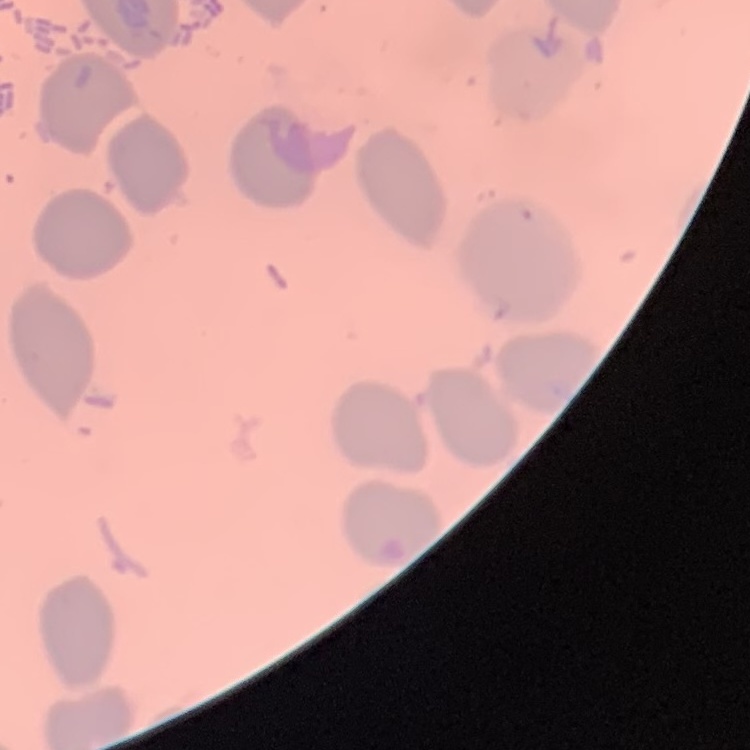
The red blood cells show no rouleaux formation. Field's or Giemsa stain. Thin peripheral smear. Square crop of a larger photomicrograph.